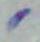
Summary:
  - Modality: micrograph
  - Magnification: 1000x
  - Identification: Toxoplasma gondii